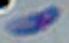

modality = micrograph
magnification = 1000x
identification = Toxoplasma gondii